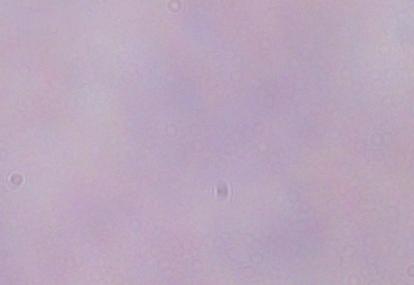
Micrograph. Captured at 1000x magnification. A trypanosome is shown.